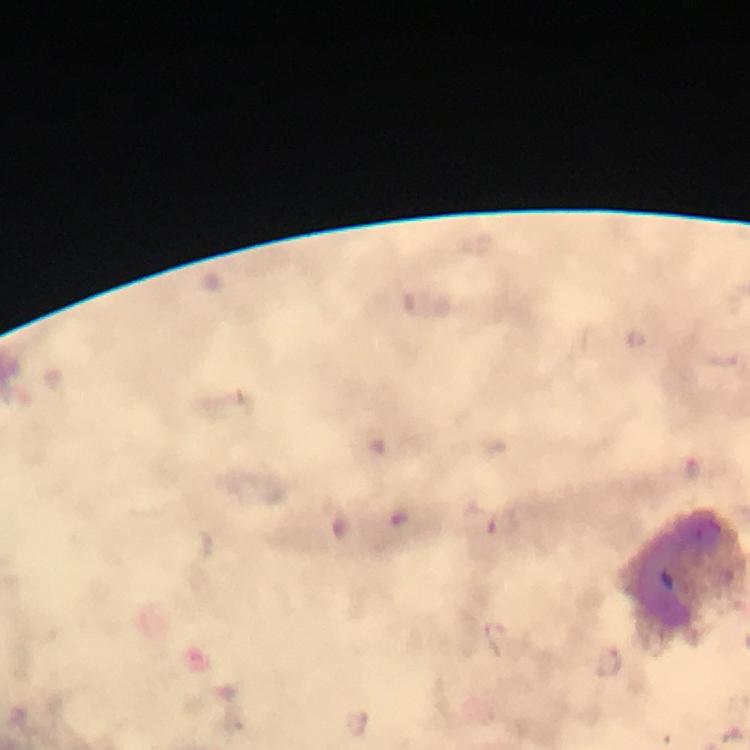
malaria parasite locations = approximate object centers, in pixels from the top-left corner: (x=504, y=523), (x=610, y=660)
cropped from = one field of view
leukocyte locations = approximate object centers, in pixels from the top-left corner: (x=683, y=576)
image size = 750×750 pixels
stain = Giemsa
magnification = 100x
immersion oil = applied
preparation = thick smear
capture = smartphone photograph through a microscope
context = from a diagnostic examination for malaria